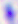

Summary:
  - Magnification: 400x
  - Identification: Toxoplasma gondii
  - Modality: photomicrograph